State which parasite is depicted.
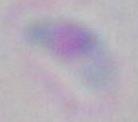

This is Toxoplasma gondii.

Summary:
  - Modality: micrograph
  - Magnification: 1000x